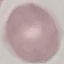

{
  "malaria_status": "uninfected",
  "preparation": "thin blood film",
  "stain": "Giemsa",
  "capture": "smartphone camera at the microscope eyepiece",
  "image_type": "cell patch, automatically extracted from a larger field of view and resized to 64 × 64 pixels"
}